Locate and identify every blood parasite.
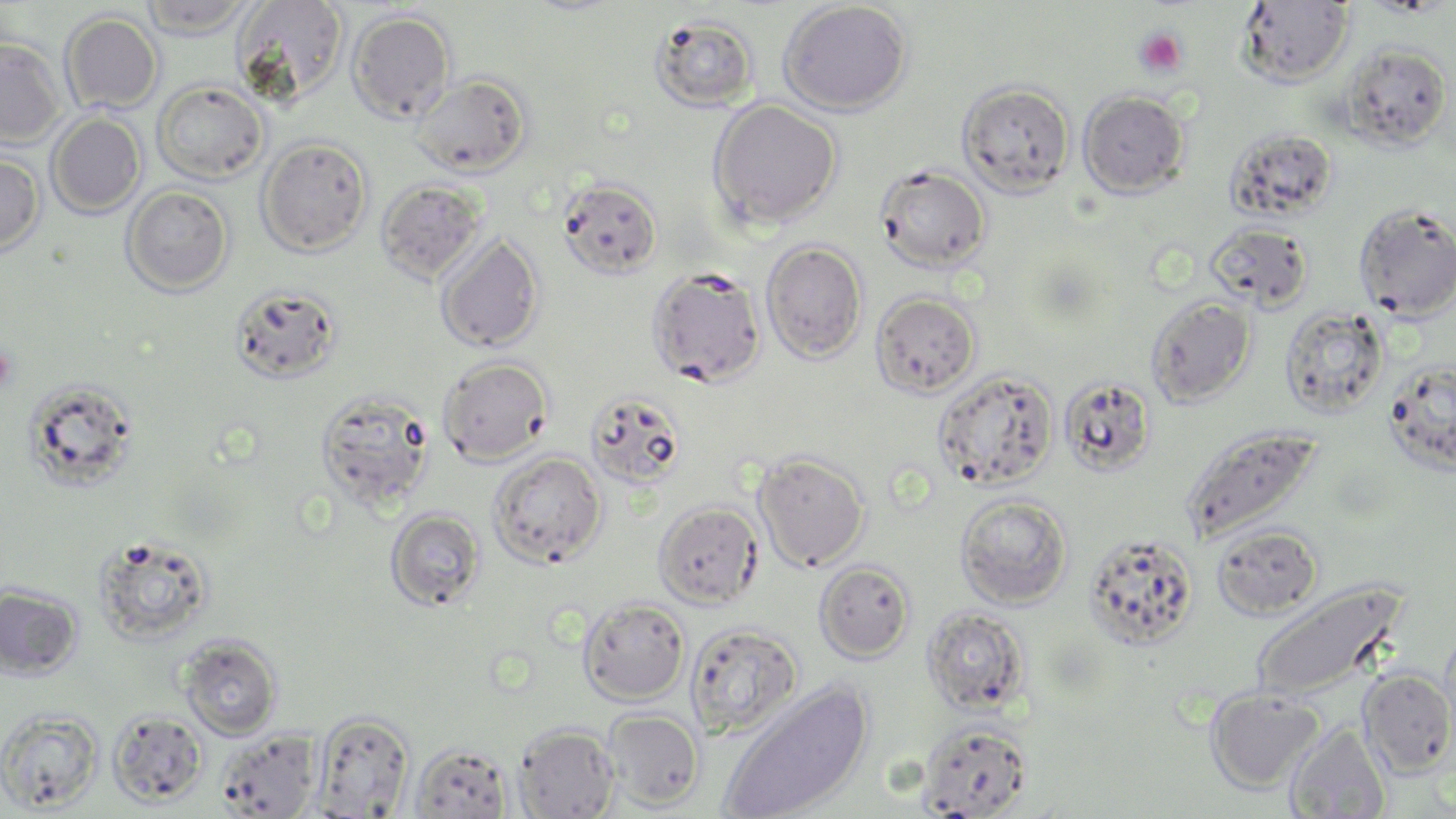

No blood parasites seen.

{
  "slide_level_diagnosis": "negative for blood parasites",
  "preparation": "thin blood film",
  "field_of_view": "one of a larger specimen",
  "uninfected_red_blood_cell_locations": "approximate bounding boxes as [x1, y1, x2, y2] in pixels: [138, 0, 258, 37], [233, 0, 348, 105], [777, 1, 912, 116], [1236, 2, 1354, 87], [347, 10, 457, 124], [59, 12, 162, 114], [648, 15, 760, 112], [0, 37, 65, 147], [1339, 43, 1452, 150], [411, 74, 531, 177], [151, 80, 269, 183], [957, 80, 1075, 197], [1078, 90, 1190, 198], [707, 99, 842, 230], [47, 113, 145, 218], [1224, 127, 1339, 223], [256, 136, 373, 257], [0, 152, 44, 257], [874, 164, 991, 272], [557, 178, 663, 279], [376, 179, 488, 283], [121, 185, 234, 296], [1352, 203, 1456, 321], [1205, 221, 1314, 312], [435, 232, 544, 353], [760, 240, 867, 364], [646, 266, 767, 388], [229, 283, 342, 384], [870, 291, 981, 398], [1145, 295, 1257, 408], [1279, 305, 1390, 419], [437, 356, 554, 465], [1383, 361, 1456, 474], [932, 369, 1058, 491], [1059, 375, 1158, 476], [23, 378, 139, 494], [314, 388, 438, 513], [585, 389, 687, 490], [1180, 424, 1323, 545], [752, 450, 871, 572], [487, 451, 607, 569], [954, 492, 1073, 608], [653, 502, 763, 609], [385, 508, 486, 611], [1211, 524, 1323, 620], [1083, 531, 1200, 650], [91, 532, 217, 647], [815, 560, 916, 663], [1249, 581, 1406, 705], [0, 583, 83, 681], [578, 597, 689, 704], [922, 605, 1031, 716], [685, 622, 803, 739], [178, 635, 283, 741], [1358, 668, 1456, 776], [717, 681, 873, 819], [1205, 688, 1325, 793], [0, 709, 104, 813], [602, 709, 704, 810], [108, 710, 208, 807], [311, 711, 414, 817], [917, 721, 1031, 818], [1284, 722, 1391, 818], [514, 723, 620, 818], [215, 730, 321, 818], [410, 743, 513, 818]",
  "image_size": "1456×819 pixels",
  "platelet_locations": "approximate bounding boxes as [x1, y1, x2, y2] in pixels: [1134, 28, 1187, 78], [0, 347, 17, 393]",
  "modality": "light microscopy",
  "stain": "May-Grünwald-Giemsa",
  "magnification": "1000x"
}